Outline each Plasmodium ovale-infected red blood cell.
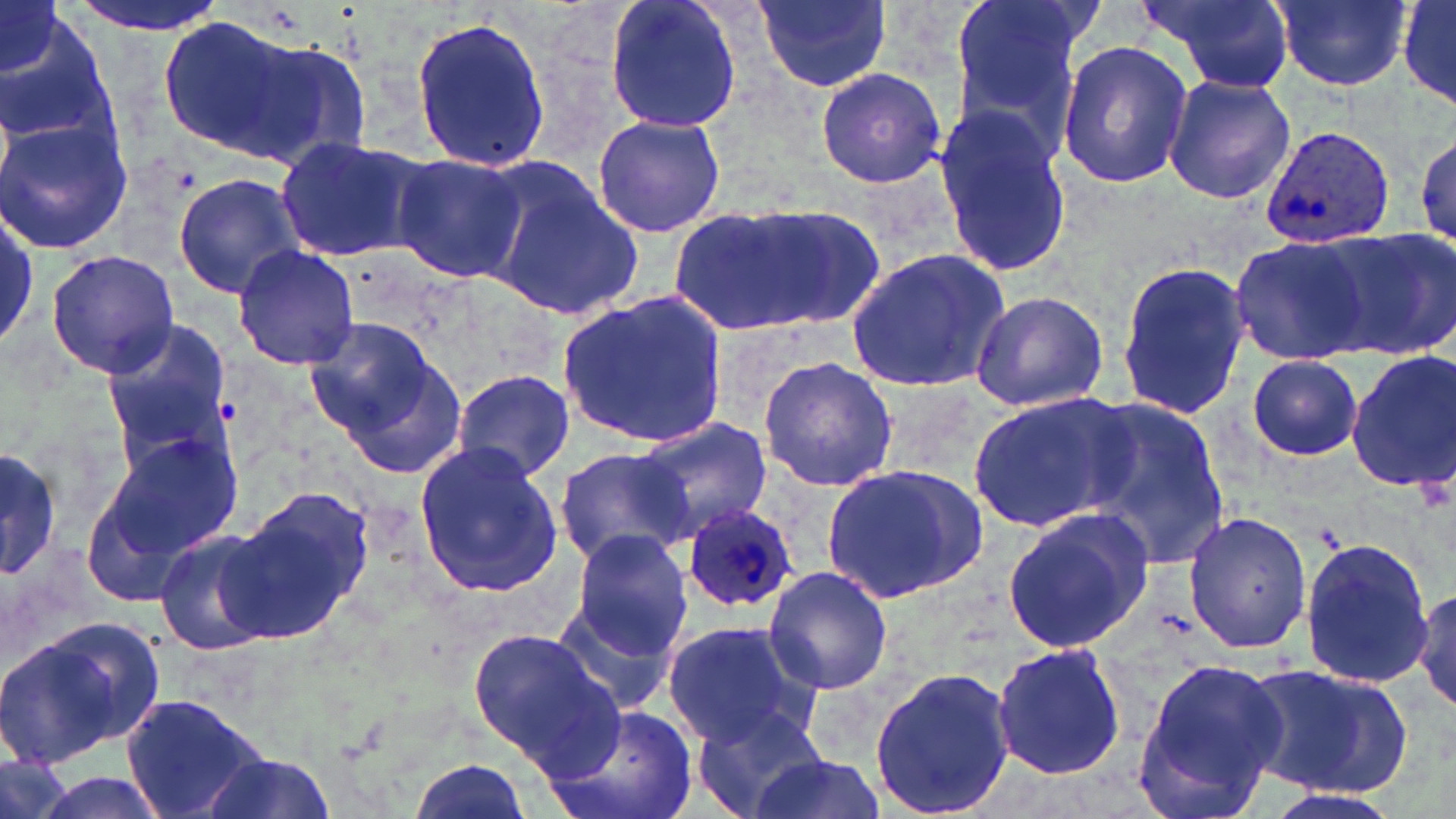

Approximate bounding boxes as [x1, y1, x2, y2] in pixels.
Plasmodium ovale-infected red blood cells: [1260, 124, 1394, 247], [680, 504, 801, 614].

Uninfected red blood cell locations: [62, 0, 232, 35], [603, 0, 744, 137], [756, 0, 891, 91], [946, 0, 1094, 159], [1137, 0, 1299, 98], [1269, 0, 1416, 94], [1395, 0, 1456, 110], [1, 2, 66, 78], [3, 9, 111, 150], [408, 14, 551, 175], [158, 16, 303, 157], [237, 31, 376, 170], [1056, 41, 1191, 188], [814, 66, 949, 189], [1163, 74, 1295, 204], [934, 100, 1069, 277], [591, 113, 727, 239], [0, 114, 132, 256], [1415, 132, 1456, 252], [275, 135, 431, 264], [389, 154, 528, 284], [481, 162, 643, 322], [173, 172, 306, 300], [666, 204, 837, 338], [1328, 227, 1455, 358], [1230, 238, 1369, 361], [231, 245, 361, 370], [843, 247, 1009, 392], [45, 250, 181, 377], [1115, 259, 1248, 422], [970, 290, 1108, 413], [559, 292, 728, 447], [308, 318, 462, 468], [98, 320, 232, 458], [1347, 351, 1456, 496], [1246, 354, 1362, 460], [757, 355, 898, 492], [450, 368, 576, 485], [965, 392, 1131, 536], [1072, 393, 1229, 571], [637, 417, 774, 544], [100, 431, 244, 564], [412, 439, 560, 599], [0, 442, 61, 585], [554, 446, 695, 566], [818, 462, 989, 604], [224, 484, 372, 644], [1000, 508, 1155, 654], [1183, 511, 1315, 655], [153, 528, 275, 656], [567, 531, 693, 659], [1298, 534, 1433, 688], [763, 566, 893, 695], [1407, 579, 1456, 717], [678, 587, 889, 721], [553, 601, 677, 717], [8, 618, 164, 763], [663, 620, 814, 748], [469, 627, 621, 775], [990, 642, 1125, 780], [1129, 658, 1289, 815], [1241, 663, 1411, 798], [868, 667, 1019, 819], [120, 693, 266, 819], [544, 702, 699, 819], [689, 704, 831, 819], [745, 748, 885, 819], [198, 751, 337, 819], [407, 756, 533, 819], [21, 767, 173, 819], [1257, 787, 1409, 819]. Slide-level diagnosis: Plasmodium ovale. Single field of view. Image is 1456×819 pixels. Captured at 1000x magnification. May-Grünwald-Giemsa-stained preparation. Thin blood film. Light microscopy.